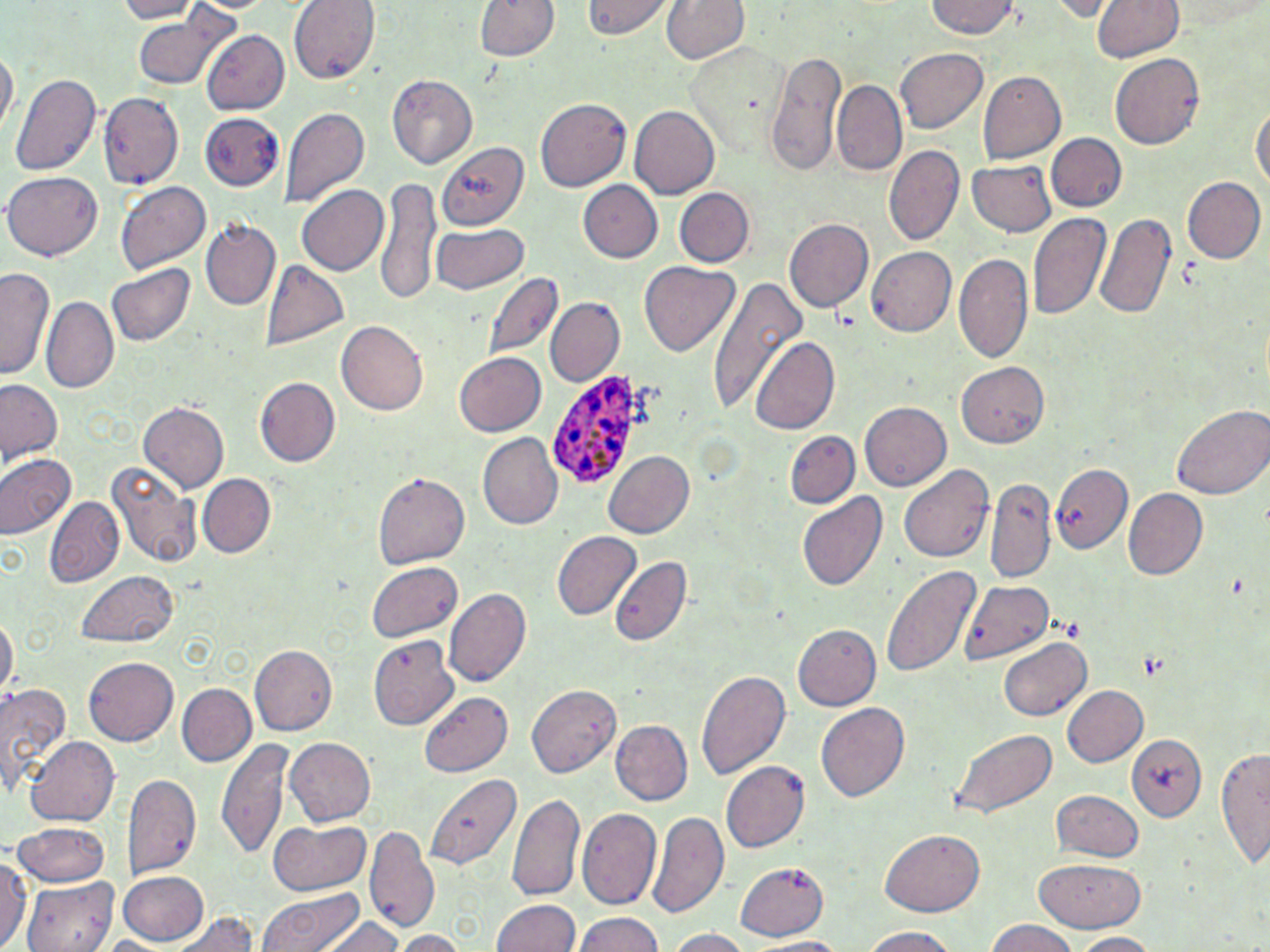 Approximate bounding boxes as (x1,y1)-(x2,y2) corner pairs in pixels. Plasmodium ovale-infected red blood cell locations: (549,367)-(641,489). Uninfected red blood cell locations: (110,0)-(200,23), (291,0)-(376,81), (474,0)-(558,62), (663,0)-(748,67), (1046,0)-(1115,21), (1087,0)-(1184,64), (582,1)-(675,41), (928,1)-(1019,40), (136,14)-(231,89), (199,30)-(292,114), (688,41)-(794,152), (0,45)-(16,136), (894,47)-(987,134), (766,51)-(847,176), (1111,52)-(1207,150), (976,71)-(1065,164), (11,72)-(100,180), (387,73)-(478,167), (833,80)-(908,175), (99,93)-(182,189), (535,97)-(629,190), (1252,100)-(1268,203), (280,105)-(368,208), (629,106)-(719,198), (201,115)-(285,189), (1046,132)-(1126,210), (444,140)-(537,229), (885,145)-(963,246), (965,158)-(1057,237), (5,172)-(104,260), (1180,174)-(1265,264), (378,179)-(445,306), (115,181)-(211,273), (579,182)-(663,263), (295,184)-(389,277), (675,188)-(751,267), (1028,211)-(1112,325), (1093,212)-(1179,323), (202,219)-(281,309), (784,219)-(874,311), (431,224)-(529,296), (867,247)-(957,337), (954,254)-(1034,366), (107,261)-(195,346), (261,262)-(351,353), (640,262)-(738,356), (1,265)-(56,382), (485,271)-(564,362), (707,278)-(807,419), (44,296)-(119,393), (544,297)-(623,386), (336,321)-(429,414), (751,335)-(843,435), (454,350)-(546,435), (956,364)-(1051,448), (254,377)-(340,468), (0,380)-(64,464), (138,401)-(229,493), (861,402)-(953,490), (1172,403)-(1270,500), (786,430)-(859,509), (477,434)-(563,530), (602,448)-(696,539), (0,452)-(75,538), (108,459)-(201,568), (899,464)-(993,563), (1051,464)-(1133,553), (195,473)-(274,559), (372,473)-(468,570), (985,478)-(1055,581), (1122,488)-(1208,581), (798,491)-(888,594), (45,496)-(124,587), (550,531)-(642,622), (608,558)-(692,645), (367,561)-(464,644), (879,566)-(981,679), (74,569)-(180,648), (958,579)-(1054,664), (446,590)-(530,686), (1,615)-(16,703), (792,624)-(879,712), (370,635)-(460,728), (1000,637)-(1091,721), (250,645)-(336,733), (83,657)-(180,745), (696,668)-(790,784), (0,682)-(72,799), (177,683)-(256,767), (523,683)-(622,780), (1060,685)-(1147,769), (421,692)-(513,778), (817,701)-(909,801), (612,719)-(693,804), (950,729)-(1056,819), (1124,732)-(1208,821), (24,735)-(117,825), (284,737)-(375,827), (216,738)-(295,859), (1215,742)-(1269,871), (722,761)-(810,853), (423,772)-(519,874), (121,773)-(201,879), (1052,789)-(1145,862), (508,792)-(584,901), (578,807)-(661,910), (648,808)-(730,921), (265,819)-(373,895), (10,823)-(112,886), (368,827)-(440,937), (880,828)-(984,915), (0,850)-(27,951), (1034,856)-(1145,933), (738,861)-(832,941), (119,870)-(213,944), (23,876)-(115,952), (256,888)-(367,952), (491,898)-(579,952), (173,909)-(260,952), (316,913)-(402,952), (573,913)-(667,952), (982,919)-(1081,952), (858,927)-(964,952), (662,929)-(756,952), (391,931)-(466,952), (1068,932)-(1164,950), (749,937)-(857,952). Slide-level diagnosis: Plasmodium ovale. Image is 1270×952 pixels. Single field of view. Captured at 1000x magnification. May-Grünwald-Giemsa-stained preparation. Thin blood smear. Light microscopy.